State which parasite is depicted.
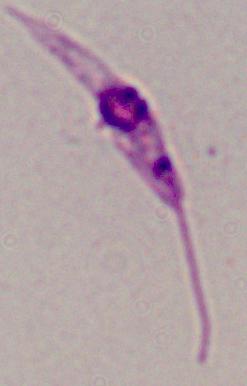

This is Leishmania.

Micrograph. Captured at 1000x magnification.